Identify the parasite.
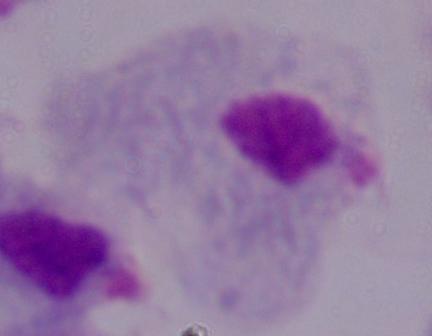

This is a trichomonad.

{
  "modality": "micrograph",
  "magnification": "1000x"
}